Locate every blood parasite and identify its species.
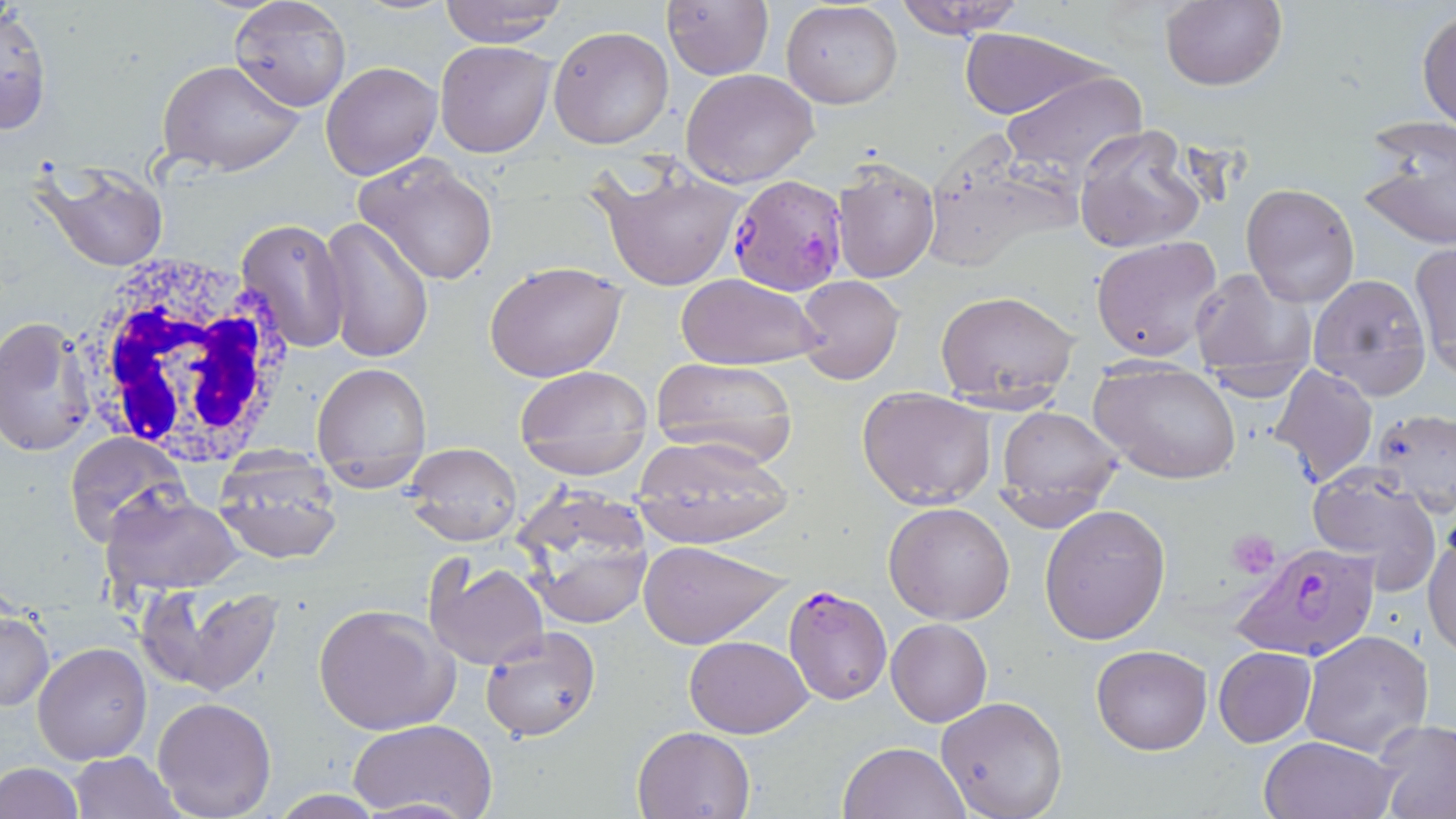
Approximate bounding boxes as (x1, y1, x2, y2) in pixels.
Plasmodium falciparum-infected red blood cells: (727, 176, 850, 296), (1230, 539, 1383, 661), (782, 585, 892, 705).
No Plasmodium ovale, Plasmodium malariae, Plasmodium vivax, Babesia divergens, or Trypanosoma brucei observed.

Summary:
  - White blood cell locations: (73, 254, 299, 467)
  - Uninfected red blood cell locations: (229, 0, 352, 113), (892, 0, 1029, 39), (436, 1, 568, 47), (782, 1, 904, 111), (1158, 1, 1288, 91), (662, 2, 773, 80), (0, 5, 53, 136), (1417, 8, 1456, 131), (548, 25, 675, 150), (958, 28, 1111, 120), (434, 39, 556, 157), (157, 59, 305, 177), (322, 61, 441, 179), (681, 69, 822, 186), (1002, 70, 1147, 181), (1357, 114, 1456, 251), (1073, 124, 1205, 255), (930, 132, 1082, 267), (352, 152, 501, 285), (829, 159, 939, 283), (30, 160, 170, 273), (591, 166, 749, 293), (1241, 182, 1361, 309), (235, 217, 350, 356), (319, 217, 433, 363), (1090, 236, 1226, 361), (1412, 243, 1456, 376), (482, 261, 628, 384), (1186, 269, 1315, 390), (674, 273, 825, 370), (1307, 273, 1431, 400), (794, 274, 905, 384), (935, 288, 1080, 405), (0, 316, 96, 458), (650, 357, 799, 464), (311, 360, 433, 489), (1089, 360, 1242, 484), (1267, 365, 1378, 487), (512, 367, 653, 446), (858, 387, 995, 509), (994, 406, 1125, 520), (1371, 407, 1456, 516), (519, 428, 653, 479), (64, 432, 191, 549), (627, 438, 793, 547), (403, 443, 521, 545), (212, 453, 342, 565), (1304, 472, 1443, 595), (99, 488, 244, 594), (514, 490, 655, 630), (883, 502, 1016, 625), (1039, 504, 1169, 646), (1424, 525, 1456, 656), (639, 540, 791, 648), (424, 556, 549, 670), (141, 581, 284, 696), (313, 603, 457, 736), (0, 610, 52, 712), (887, 619, 992, 727), (479, 625, 603, 741), (1300, 629, 1434, 756), (684, 635, 813, 738), (33, 642, 151, 765), (1091, 644, 1211, 756), (1213, 647, 1316, 746), (936, 695, 1069, 818), (151, 697, 276, 819), (350, 719, 497, 819), (1372, 720, 1456, 816), (632, 727, 754, 818), (1260, 737, 1397, 819), (839, 740, 971, 819), (68, 751, 180, 818), (0, 760, 83, 819), (351, 797, 482, 817)
  - Platelet locations: (1228, 526, 1278, 579)
  - Slide-level diagnosis: Plasmodium falciparum
  - Modality: light microscopy
  - Stain: May-Grünwald-Giemsa
  - Preparation: thin blood film
  - Magnification: 1000x
  - Image size: 1456×819 pixels
  - Field of view: single